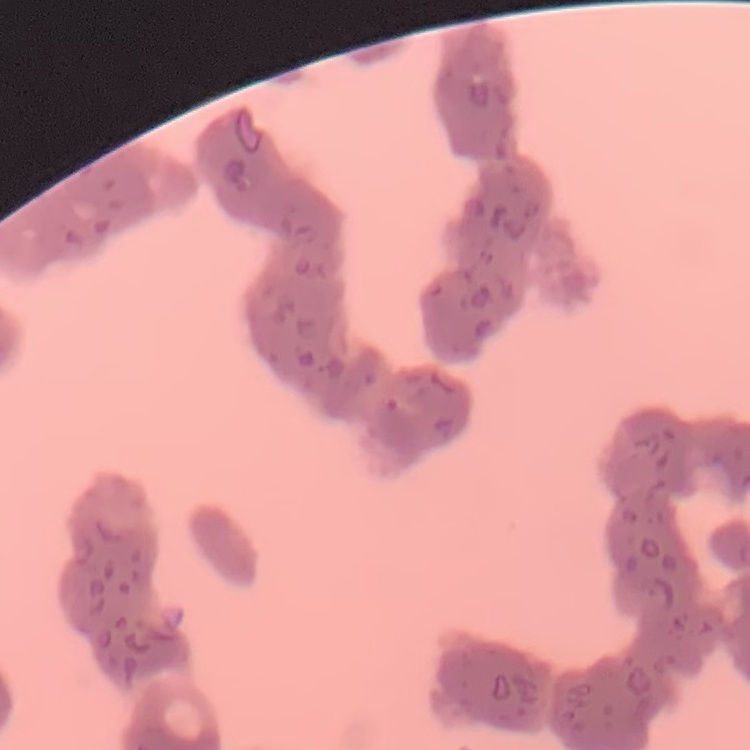
The erythrocytes exhibit rouleaux formation. Field's or Giemsa stain. Square crop of a larger photomicrograph. Thin peripheral smear.